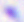

Summary:
  - Identification: Toxoplasma gondii
  - Modality: micrograph
  - Magnification: 400x